Assess the morphology of the erythrocytes.
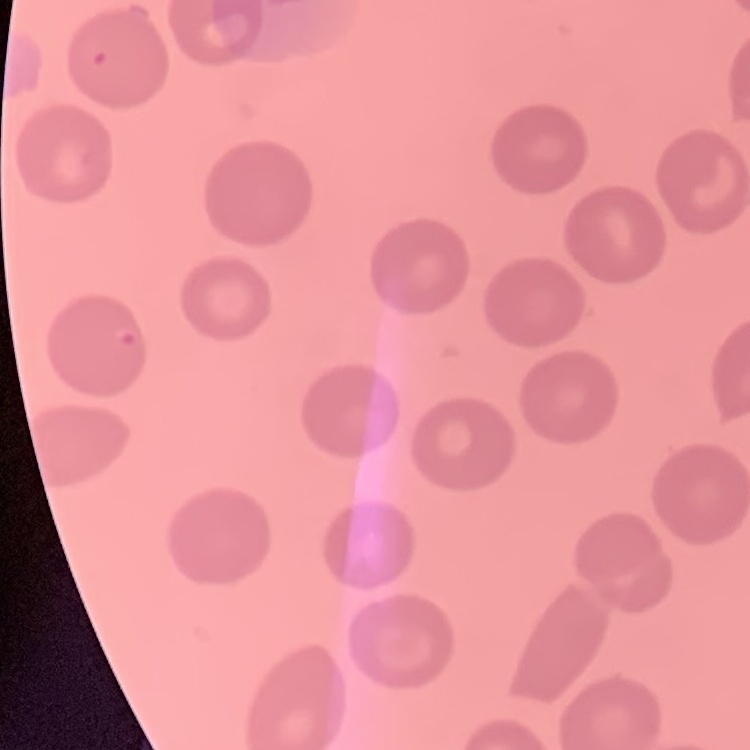
They show no rouleaux formation.

Square crop of a larger photomicrograph. Thin blood smear. Stained with either Field's or Giemsa.